Give the position of every Plasmodium parasite visible.
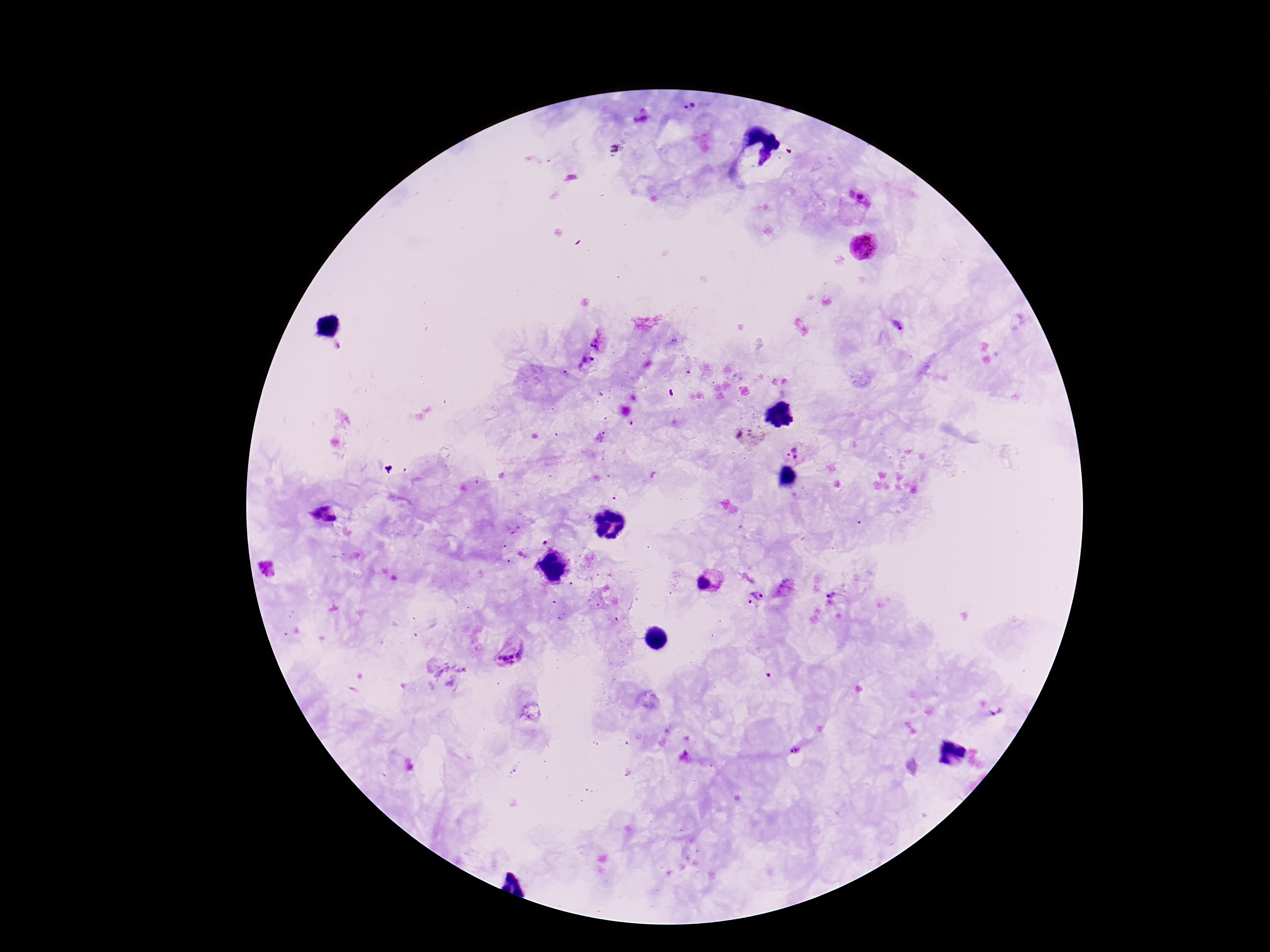
Approximate centers as {x, y} in pixels.
Plasmodium parasites: {690, 107}, {859, 197}, {864, 248}, {897, 326}, {598, 343}, {588, 363}, {793, 452}, {325, 506}, {314, 514}, {330, 519}, {545, 542}, {703, 583}, {782, 586}, {758, 593}, {831, 597}, {749, 601}, {509, 652}, {994, 711}, {796, 749}.

magnification = 100x
stain = Giemsa
image size = 1270×952 pixels
field of view = single
preparation = thick blood film
patient malaria status = positive
capture = smartphone camera through the microscope eyepiece